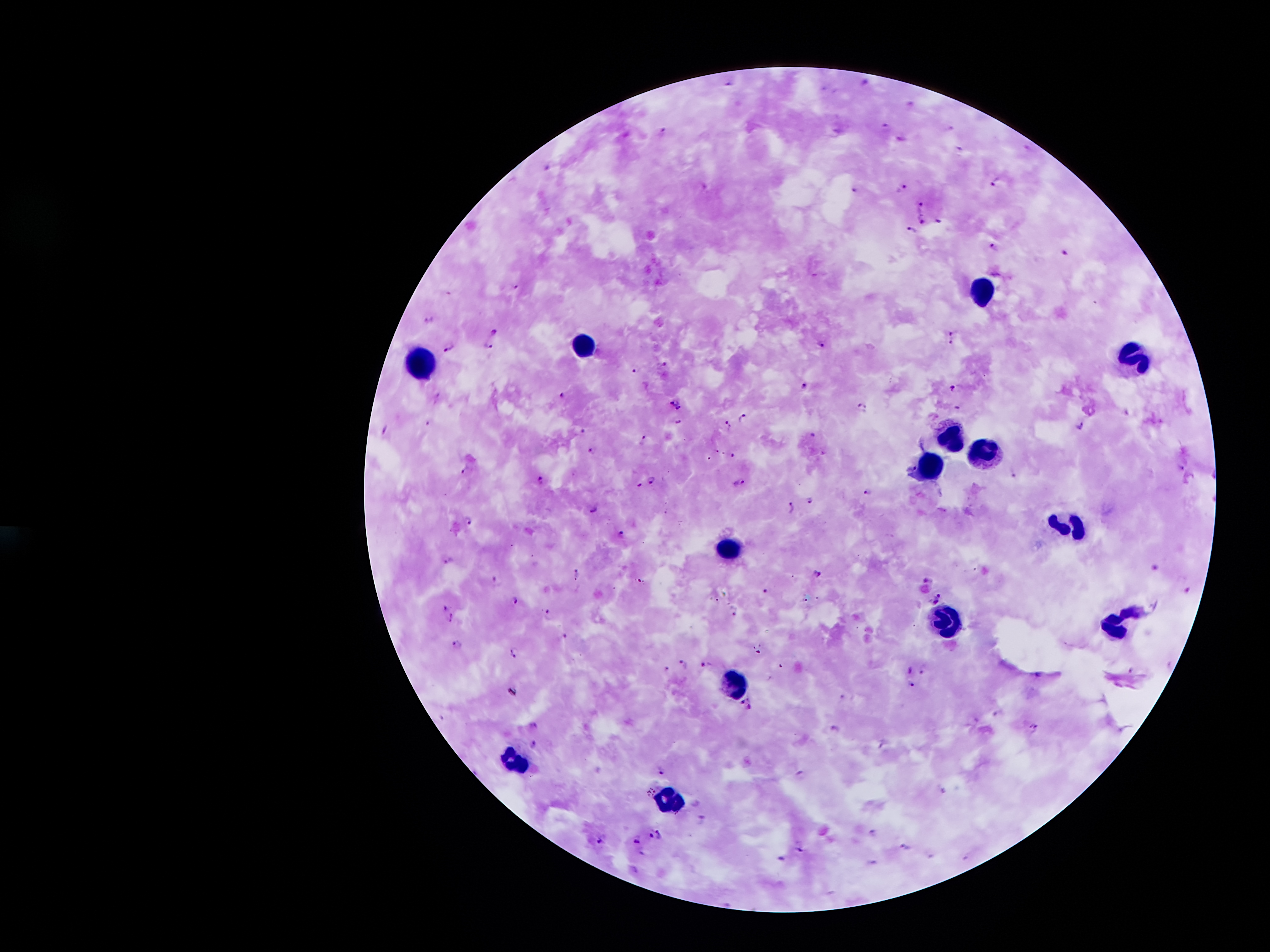
coordinate format = approximate centers as {x, y} in pixels
malaria parasite locations = {729, 84}, {886, 127}, {662, 131}, {900, 138}, {961, 150}, {548, 167}, {997, 181}, {902, 188}, {855, 190}, {923, 206}, {923, 220}, {940, 220}, {912, 231}, {996, 246}, {1063, 256}, {517, 286}, {430, 321}, {494, 330}, {954, 332}, {823, 343}, {951, 344}, {488, 347}, {451, 348}, {665, 364}, {635, 370}, {804, 386}, {954, 386}, {563, 394}, {676, 403}, {863, 405}, {959, 408}, {742, 418}, {679, 422}, {1081, 424}, {729, 426}, {385, 431}, {582, 431}, {812, 435}, {644, 438}, {593, 450}, {734, 455}, {910, 466}, {1181, 467}, {463, 469}, {1014, 475}, {653, 479}, {540, 480}, {739, 483}, {640, 485}, {867, 491}, {809, 500}, {792, 508}, {594, 509}, {469, 520}, {621, 533}, {450, 561}, {1157, 567}, {578, 573}, {818, 574}, {497, 580}, {929, 580}, {767, 591}, {1188, 591}, {941, 596}, {514, 601}, {935, 602}, {444, 608}, {736, 613}, {548, 614}, {451, 618}, {563, 638}, {457, 645}, {515, 653}, {686, 664}, {708, 665}, {668, 670}, {911, 670}, {926, 670}, {912, 684}, {843, 697}, {746, 704}, {535, 725}, {1034, 726}, {535, 745}, {663, 772}, {801, 775}, {704, 819}, {873, 833}, {660, 834}, {651, 836}, {599, 840}, {637, 842}, {907, 848}, {802, 849}, {643, 855}, {782, 859}
leukocyte locations = {979, 289}, {586, 344}, {1136, 360}, {422, 366}, {948, 436}, {985, 450}, {929, 469}, {1069, 524}, {728, 542}, {952, 619}, {1119, 621}, {736, 680}, {514, 759}, {667, 798}
field of view = one from this slide
preparation = thick blood film
stain = Giemsa
capture = smartphone through the microscope eyepiece
image size = 1270×952 pixels
magnification = 100x
patient malaria status = positive for Plasmodium falciparum